Report the malaria status of this cell.
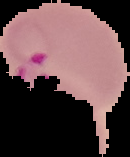

It is parasitized.

Summary:
  - Image size: 130×157 pixels
  - Image type: segmented cell region with the area outside set to black
  - Preparation: thin blood film